Report the malaria status of this cell.
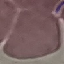

It is uninfected.

Automatically extracted cell patch, resized to 64 × 64 pixels. Photographed with a smartphone camera at the microscope eyepiece. Thin smear of blood. Giemsa-stained preparation.